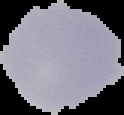

Image is 124×115 pixels. Malaria status: uninfected. Segmented cell region on a black background. From a thin blood film.